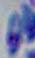
Summary:
  - Identification: Toxoplasma gondii
  - Magnification: 1000x
  - Modality: photomicrograph